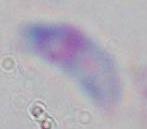

Summary:
  - Identification: Toxoplasma gondii
  - Modality: micrograph
  - Magnification: 1000x